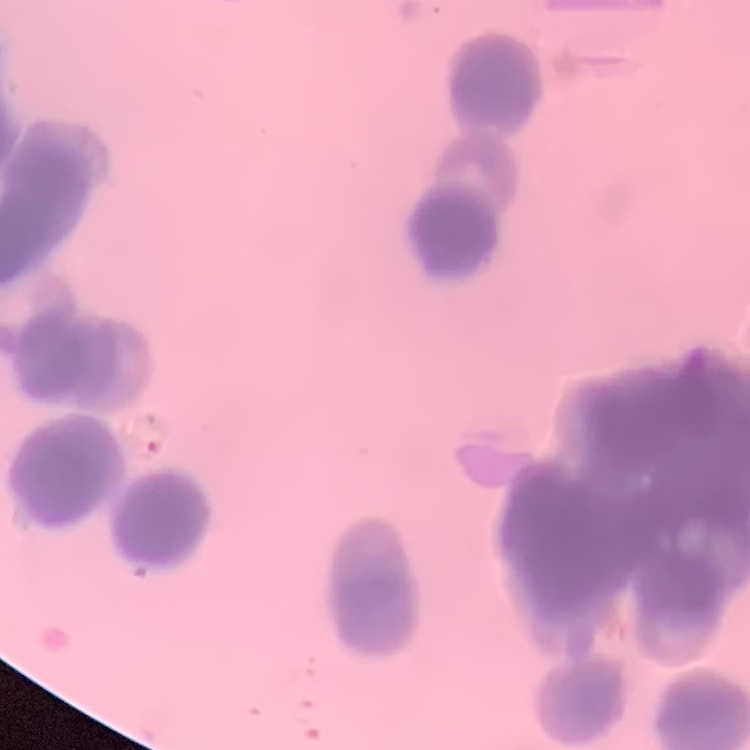 The erythrocytes exhibit rouleaux formation. One tile cut from a larger photomicrograph. Field's or Giemsa stain. Thin blood smear.